Comment on the morphology of the erythrocytes.
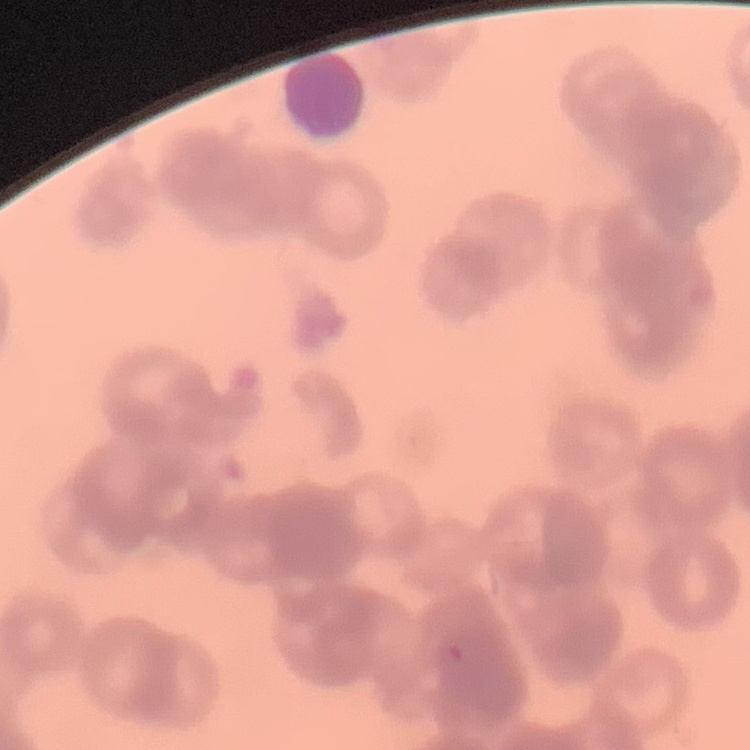
They show rouleaux formation.

Summary:
  - Preparation: thin blood film
  - Image type: square crop of a larger photomicrograph
  - Stain: Field's or Giemsa